State which parasite is depicted.
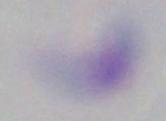

Toxoplasma gondii.

Photomicrograph. 1000x magnification.